Point out each Plasmodium parasite.
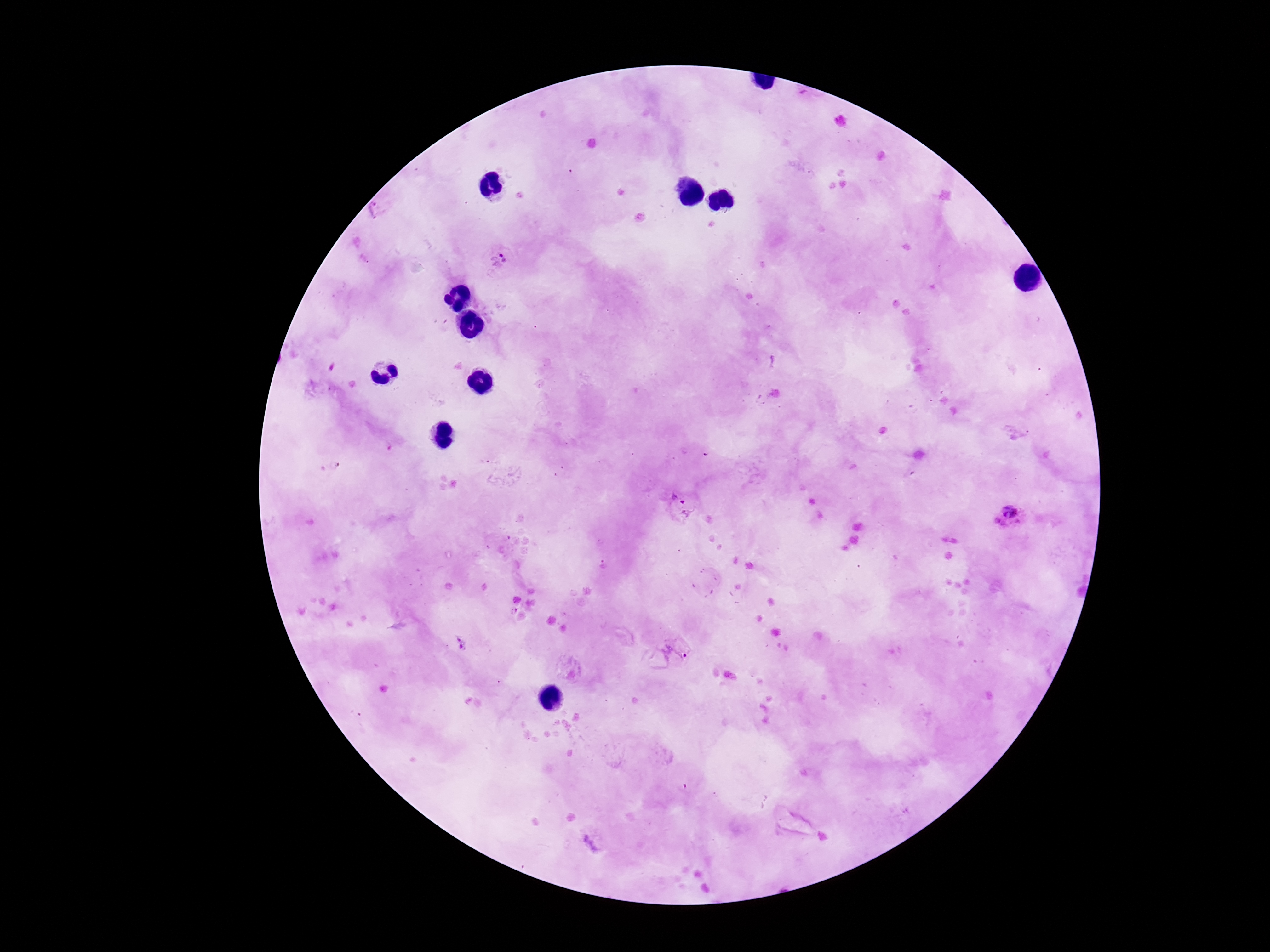
Approximate object centers, in pixels from the top-left corner.
Plasmodium parasites: (x=500, y=259), (x=681, y=505), (x=1009, y=515), (x=461, y=642), (x=669, y=655).

Giemsa-stained preparation. Thick peripheral-blood smear. 100x magnification. Smartphone photograph taken through the microscope eyepiece. Image is 1270×952 pixels. Patient malaria status: infected. One field from this slide.